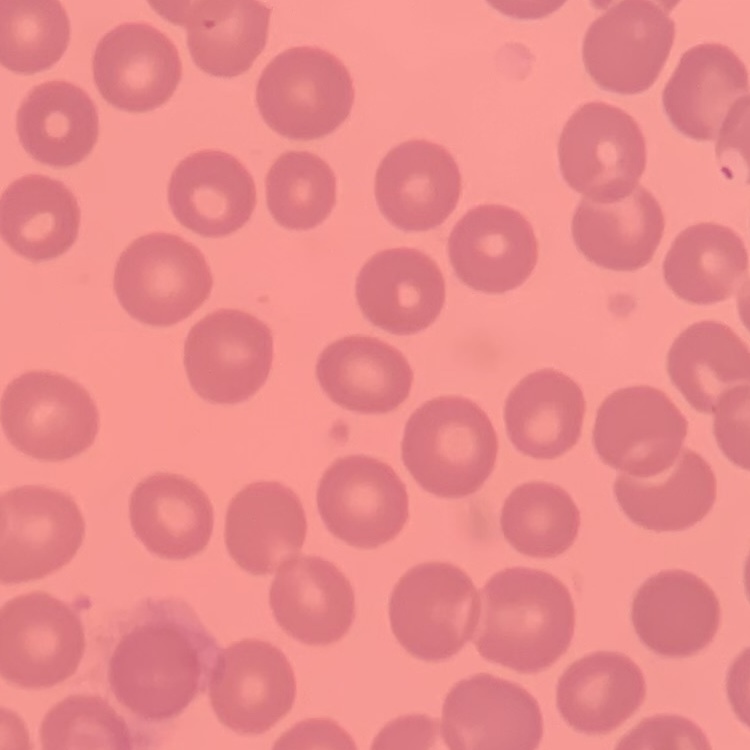
red blood cell morphology = no rouleaux formation
image type = one tile cut from a larger photomicrograph
stain = Field's or Giemsa
preparation = thin blood film